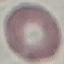

Result: no malaria parasites seen. Photographed with a smartphone camera at the microscope eyepiece. Giemsa-stained preparation. Thin blood smear. Cell patch, automatically extracted from a larger field of view and resized to 64 × 64 pixels.